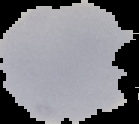

{
  "preparation": "thin blood film",
  "image_size": "139×124 pixels",
  "image_type": "cell region segmented out of the field of view; surrounding area masked to black",
  "malaria_status": "uninfected"
}